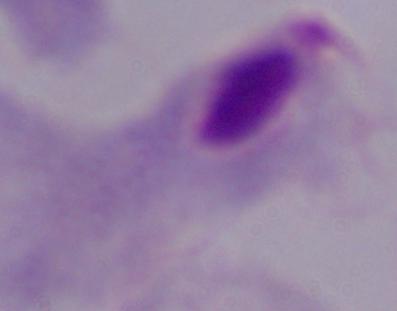
identification = trichomonad
magnification = 1000x
modality = micrograph